Classify this cell by malaria status.
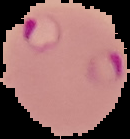

It is parasitized.

Segmented cell region on a black background. Image is 130×139 pixels. From a thin blood smear.